Classify this cell by malaria status.
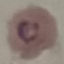

Parasitized.

{
  "capture": "smartphone through the microscope eyepiece",
  "preparation": "thin blood film",
  "image_type": "automatically extracted cell patch, resized to 64 × 64 pixels",
  "stain": "Giemsa"
}